Comment on the morphology of the erythrocytes.
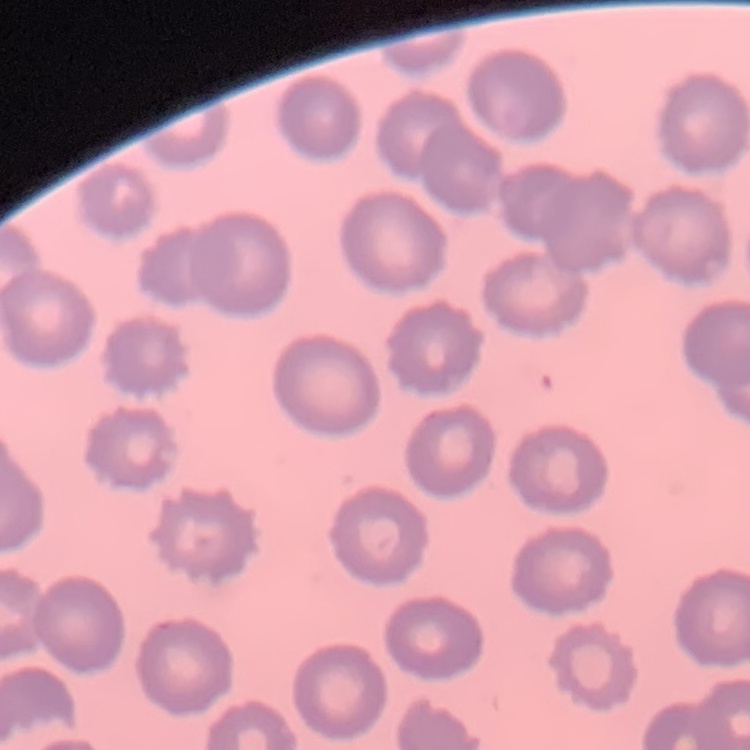

No rouleaux formation.

{
  "stain": "Field's or Giemsa",
  "preparation": "thin blood smear",
  "image_type": "square crop of a larger photomicrograph"
}